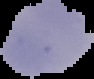 Image is 94×79 pixels. Malaria status: uninfected. The area outside the segmented cell region is set to black. From a thin blood smear.